Describe the morphology of the red blood cells.
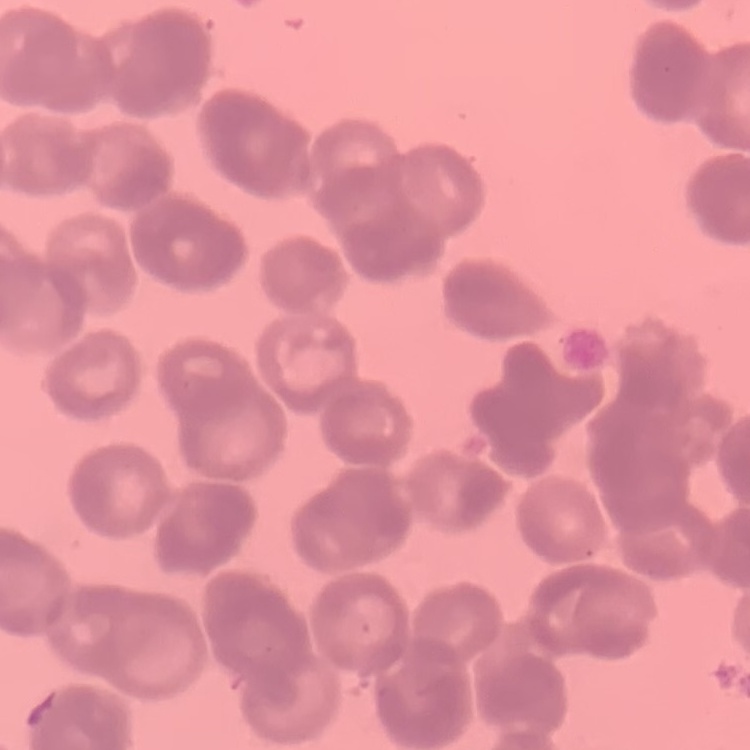

They show rouleaux formation.

Field's or Giemsa stain. One tile cut from a larger photomicrograph. Thin peripheral smear.